Assess this cell for malaria.
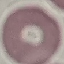
It is uninfected.

capture = smartphone camera at the microscope eyepiece
image type = cell patch, automatically extracted from a larger field of view and resized to 64 × 64 pixels
preparation = thin blood smear
stain = Giemsa